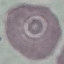 Result: no malaria parasites detected. Photographed with a smartphone camera at the microscope eyepiece. Automatically extracted cell patch, resized to 64 × 64 pixels. Giemsa-stained preparation. Thin blood film.